Describe the morphology of the red blood cells.
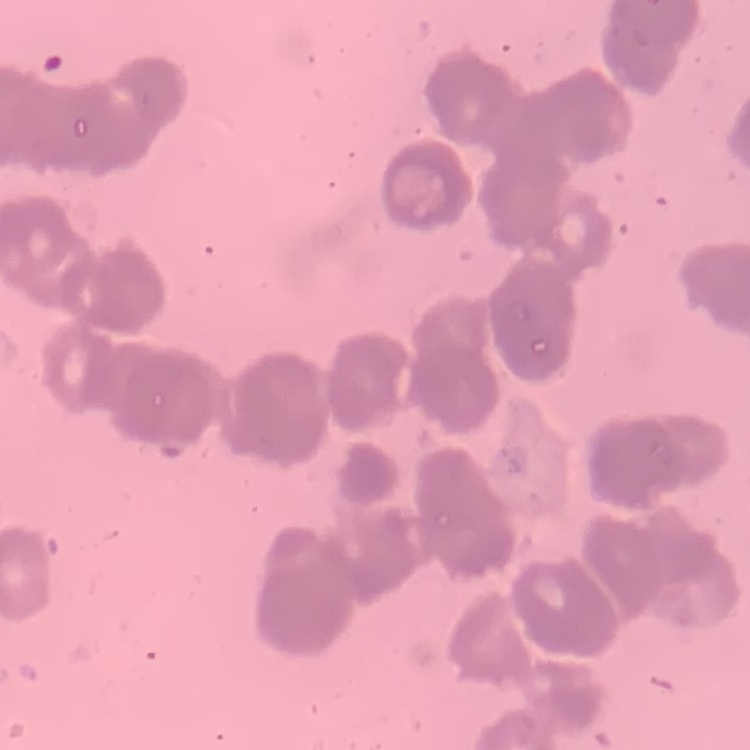
They show rouleaux formation.

Summary:
  - Stain: Field's or Giemsa
  - Image type: square crop of a larger photomicrograph
  - Preparation: thin peripheral smear